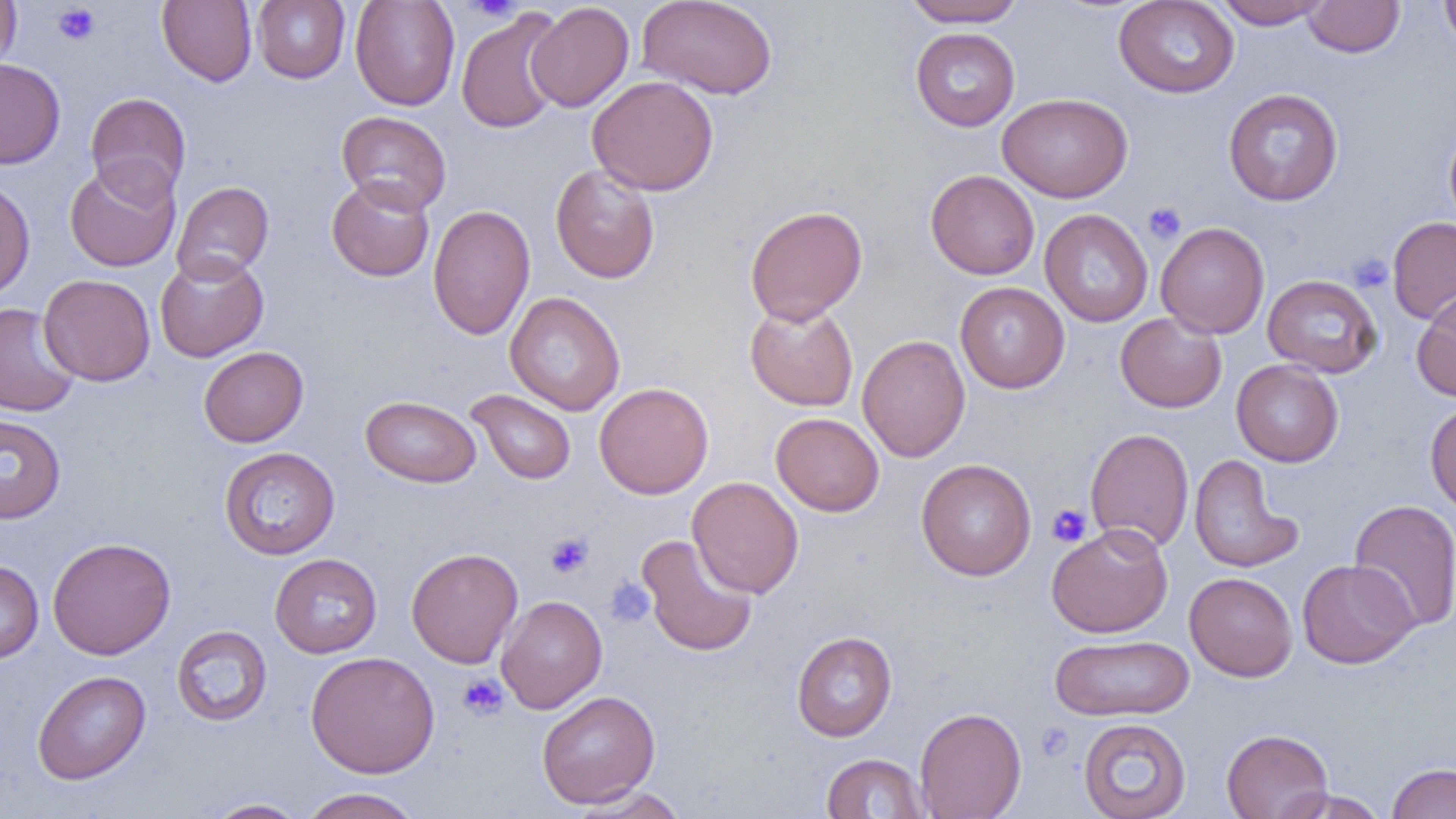
Summary:
  - Coordinate format: approximate bounding boxes as [x1, y1, x2, y2] in pixels
  - Uninfected red blood cell locations: [0, 0, 20, 77], [157, 0, 257, 87], [252, 0, 350, 84], [350, 0, 460, 111], [637, 0, 778, 100], [1113, 0, 1240, 98], [1213, 0, 1331, 29], [1439, 0, 1456, 50], [902, 1, 1027, 28], [1302, 1, 1405, 57], [525, 2, 634, 112], [455, 8, 567, 134], [910, 27, 1020, 131], [0, 58, 66, 170], [587, 75, 719, 196], [1223, 88, 1344, 206], [85, 92, 191, 204], [998, 92, 1133, 202], [337, 110, 451, 215], [1444, 122, 1456, 233], [64, 160, 180, 272], [549, 163, 660, 284], [925, 169, 1040, 280], [326, 176, 435, 282], [0, 178, 35, 300], [172, 181, 274, 283], [428, 204, 535, 340], [744, 205, 868, 324], [1039, 209, 1153, 327], [1387, 217, 1456, 324], [1155, 222, 1270, 338], [154, 253, 269, 362], [38, 274, 155, 386], [1262, 274, 1383, 378], [955, 281, 1070, 393], [1412, 288, 1456, 402], [505, 292, 626, 415], [744, 301, 859, 411], [0, 303, 80, 417], [1115, 312, 1227, 413], [857, 335, 970, 462], [198, 346, 309, 447], [1231, 359, 1343, 467], [594, 382, 713, 499], [466, 389, 576, 484], [360, 395, 481, 487], [1424, 400, 1456, 515], [771, 412, 884, 516], [0, 414, 66, 524], [1085, 427, 1194, 552], [219, 447, 340, 560], [1188, 453, 1302, 573], [915, 459, 1036, 580], [688, 476, 804, 598], [1348, 499, 1456, 633], [1045, 522, 1173, 638], [636, 534, 758, 657], [47, 537, 176, 660], [406, 547, 523, 668], [270, 552, 382, 658], [1297, 558, 1418, 669], [0, 560, 43, 664], [1184, 572, 1298, 681], [496, 595, 607, 713], [171, 625, 273, 727], [791, 631, 897, 742], [1050, 634, 1195, 721], [305, 651, 440, 777], [31, 670, 151, 785], [536, 690, 660, 808], [914, 707, 1027, 818], [1077, 717, 1192, 819], [1221, 728, 1333, 818], [820, 752, 931, 818], [1386, 763, 1456, 819], [569, 785, 688, 818], [299, 787, 424, 819], [1275, 788, 1388, 818], [202, 798, 309, 818]
  - Platelet locations: [463, 0, 524, 22], [52, 3, 100, 45], [1142, 202, 1186, 244], [1347, 253, 1393, 293], [1046, 503, 1092, 547], [545, 531, 594, 578], [605, 578, 654, 626], [457, 674, 509, 721], [1035, 723, 1074, 762]
  - Slide-level diagnosis: negative for blood parasites
  - Modality: optical microscopy
  - Magnification: 1000x
  - Field of view: one of a larger specimen
  - Preparation: thin blood smear
  - Image size: 1456×819 pixels